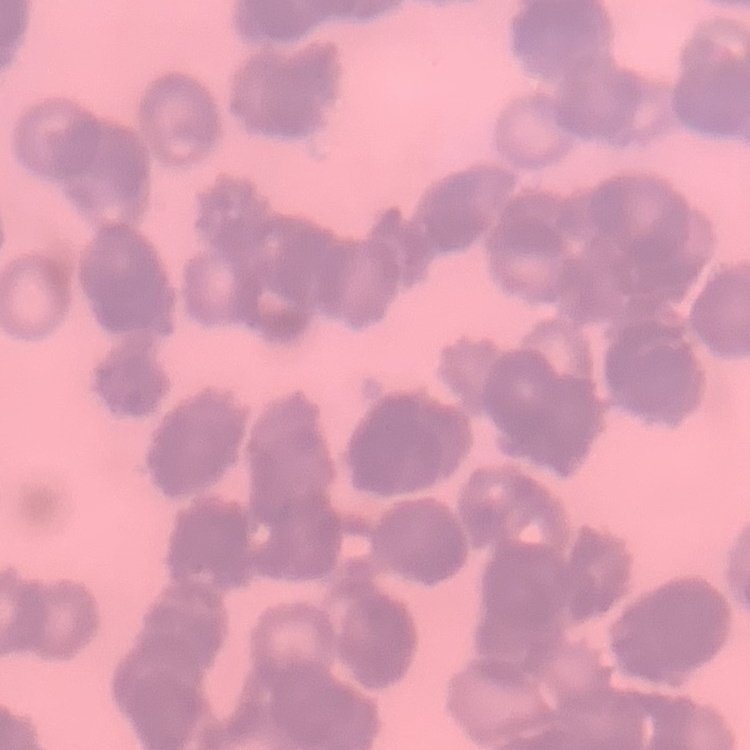

red blood cell morphology = rouleaux formation
image type = square crop of a larger photomicrograph
stain = Field's or Giemsa
preparation = thin blood film